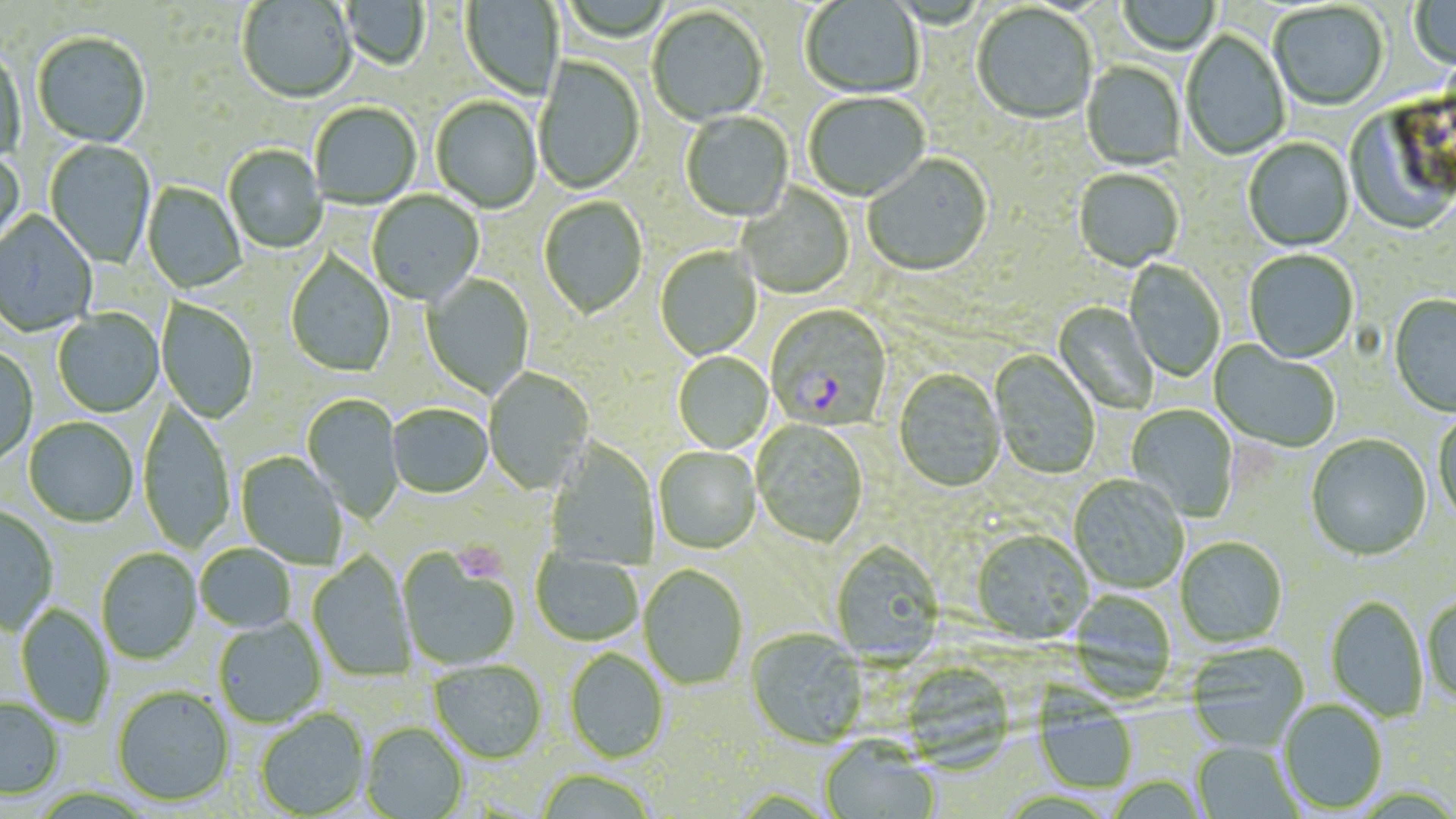

Summary:
  - Coordinate format: approximate bounding boxes as [x1, y1, x2, y2] in pixels
  - Plasmodium falciparum-infected red blood cell locations: [766, 306, 893, 432]
  - Platelet locations: [454, 541, 506, 583]
  - Uninfected red blood cell locations: [1118, 0, 1221, 56], [1409, 0, 1456, 71], [237, 1, 357, 105], [340, 1, 429, 72], [460, 1, 564, 102], [800, 1, 924, 99], [1270, 3, 1388, 112], [972, 5, 1097, 126], [646, 7, 768, 127], [1181, 30, 1291, 161], [33, 34, 151, 149], [0, 49, 26, 166], [534, 56, 645, 195], [1082, 62, 1186, 172], [804, 93, 930, 203], [431, 97, 542, 214], [309, 103, 422, 210], [1342, 105, 1455, 237], [680, 112, 794, 223], [1243, 138, 1354, 253], [45, 139, 156, 269], [223, 145, 327, 254], [0, 150, 26, 257], [863, 155, 993, 278], [1073, 169, 1183, 273], [142, 183, 246, 294], [737, 184, 855, 300], [367, 191, 484, 307], [539, 197, 648, 321], [0, 211, 98, 337], [655, 247, 762, 361], [1244, 251, 1358, 365], [285, 252, 395, 377], [1124, 259, 1225, 382], [422, 275, 534, 399], [1388, 295, 1456, 418], [157, 300, 258, 424], [1052, 302, 1158, 414], [53, 309, 164, 417], [1208, 339, 1340, 452], [0, 347, 38, 466], [989, 350, 1100, 480], [672, 352, 774, 454], [484, 367, 594, 495], [893, 370, 1006, 493], [301, 394, 403, 523], [138, 400, 235, 553], [1125, 404, 1239, 522], [387, 405, 492, 499], [1432, 411, 1456, 525], [24, 418, 139, 528], [751, 421, 868, 548], [1306, 434, 1432, 562], [546, 441, 660, 569], [653, 448, 761, 555], [235, 452, 347, 569], [1068, 476, 1188, 594], [0, 506, 58, 635], [971, 532, 1093, 646], [1176, 538, 1287, 648], [830, 543, 944, 667], [195, 544, 297, 634], [96, 549, 202, 664], [530, 549, 643, 647], [397, 550, 521, 671], [308, 552, 416, 681], [638, 566, 748, 691], [1069, 589, 1176, 699], [1326, 596, 1428, 723], [1423, 596, 1456, 708], [16, 603, 114, 728], [214, 617, 327, 728], [745, 630, 868, 751], [1186, 643, 1309, 752], [564, 650, 669, 764], [429, 661, 546, 765], [112, 686, 235, 808], [0, 697, 64, 800], [1278, 700, 1387, 814], [1035, 702, 1138, 794], [255, 710, 371, 818], [361, 724, 469, 819], [820, 739, 940, 819], [1192, 741, 1301, 819], [535, 769, 659, 818], [1105, 776, 1209, 818]
  - Slide-level diagnosis: Plasmodium falciparum
  - Field of view: single
  - Preparation: thin blood film
  - Stain: May-Grünwald-Giemsa
  - Magnification: 1000x
  - Modality: light microscopy
  - Image size: 1456×819 pixels